Comment on the morphology of the red blood cells.
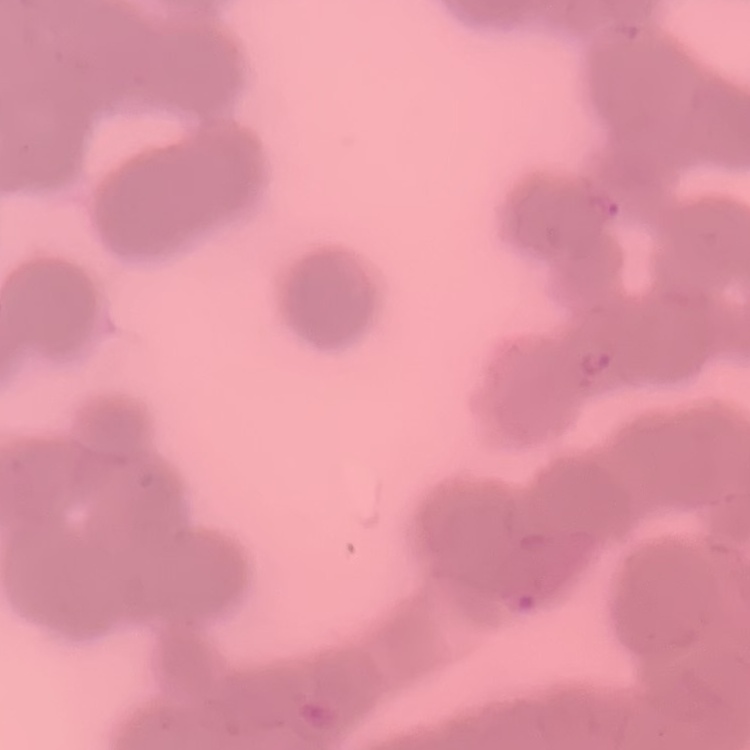
Rouleaux formation.

{
  "stain": "Field's or Giemsa",
  "image_type": "one tile cut from a larger photomicrograph",
  "preparation": "thin blood film"
}